Locate every Babesia divergens-infected red blood cell.
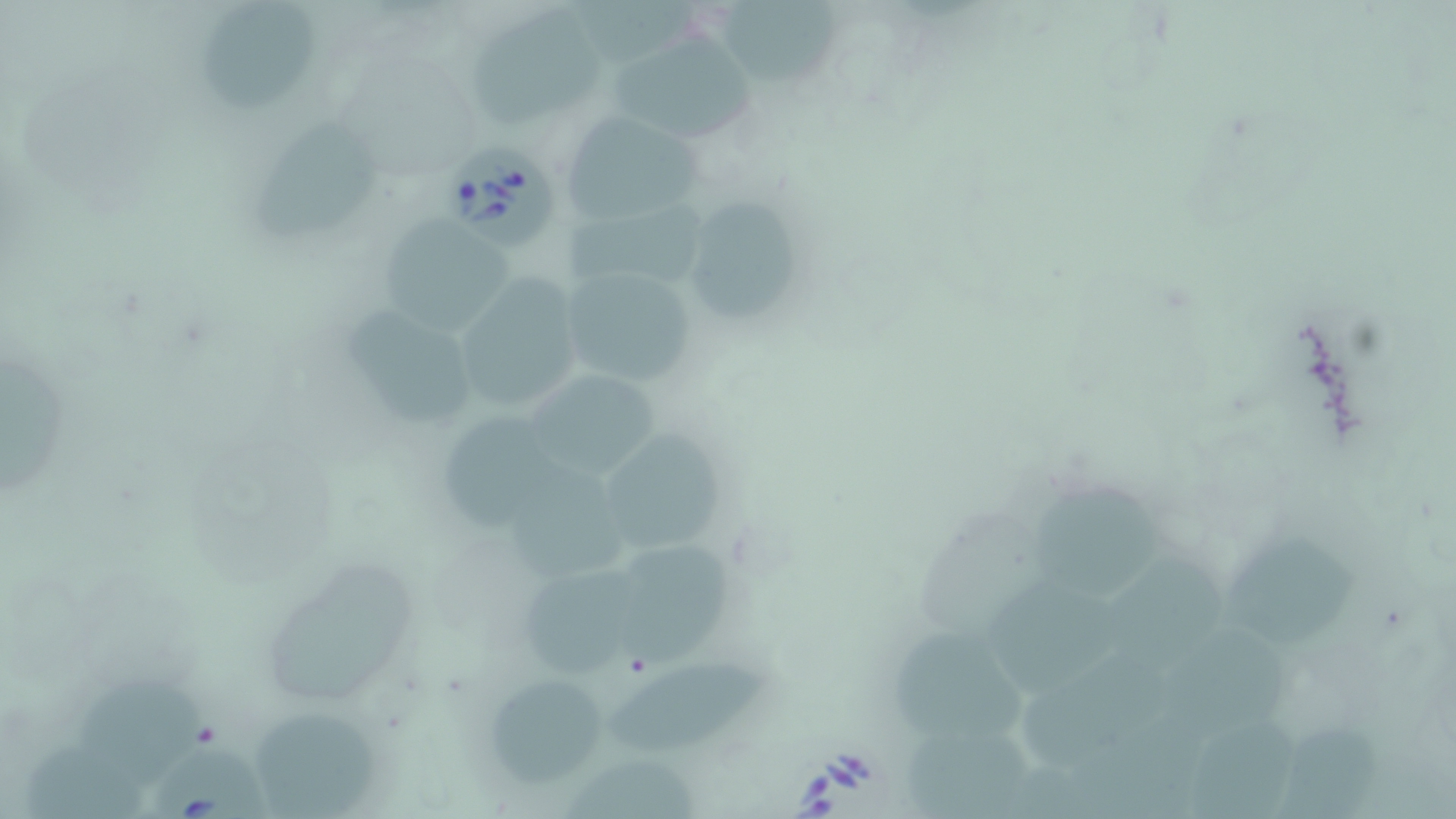

Approximate bounding boxes as [x1, y1, x2, y2] in pixels.
Babesia divergens-infected red blood cells: [449, 142, 561, 249], [149, 737, 274, 819].

Uninfected red blood cell locations: [200, 0, 324, 111], [721, 0, 844, 92], [470, 8, 607, 126], [610, 29, 759, 150], [562, 109, 704, 221], [250, 118, 380, 239], [670, 192, 811, 330], [565, 200, 714, 290], [372, 212, 513, 335], [557, 266, 702, 387], [443, 272, 590, 412], [343, 303, 478, 425], [5, 362, 68, 504], [531, 370, 659, 481], [440, 410, 568, 539], [607, 433, 724, 552], [513, 463, 635, 581], [1034, 477, 1157, 603], [1220, 534, 1355, 655], [624, 545, 727, 660], [1112, 554, 1231, 675], [267, 558, 420, 700], [524, 563, 638, 680], [990, 578, 1121, 698], [1161, 625, 1290, 735], [893, 630, 1026, 739], [607, 657, 767, 757], [76, 669, 205, 780], [490, 671, 605, 787], [259, 710, 371, 819], [1281, 722, 1387, 819], [905, 724, 1045, 819], [26, 738, 143, 819], [563, 759, 698, 819]. Slide-level diagnosis: Babesia divergens. Light microscopy. Thin blood film. May-Grünwald-Giemsa-stained preparation. Single field of view. Image is 1456×819 pixels. Captured at 1000x magnification.